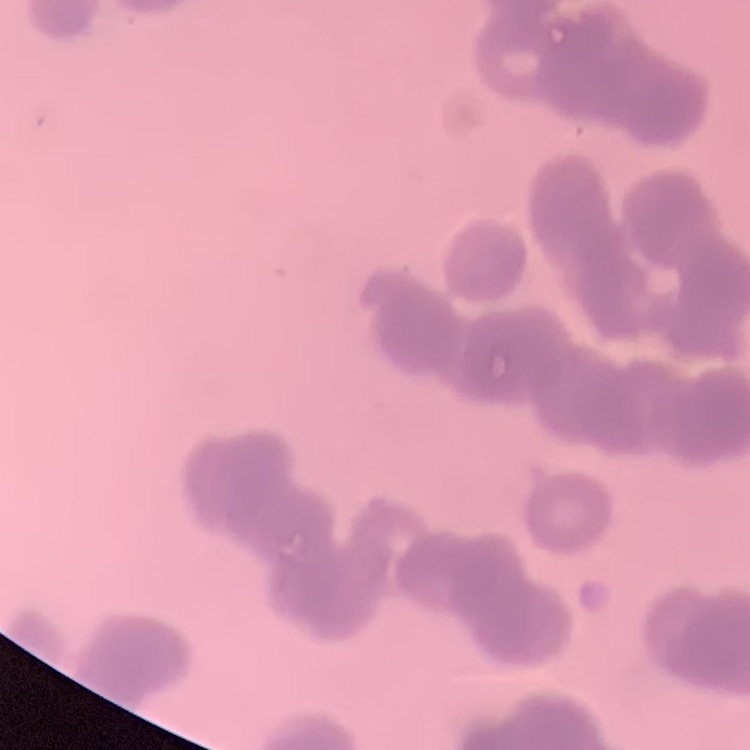

red blood cell morphology = rouleaux formation
image type = square crop of a larger photomicrograph
preparation = thin blood film
stain = Field's or Giemsa